State which parasite is depicted.
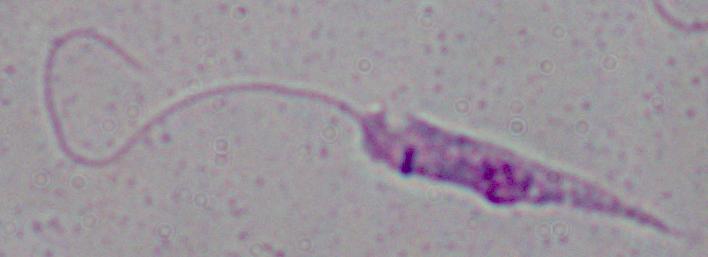
Leishmania.

Photomicrograph. 1000x magnification.